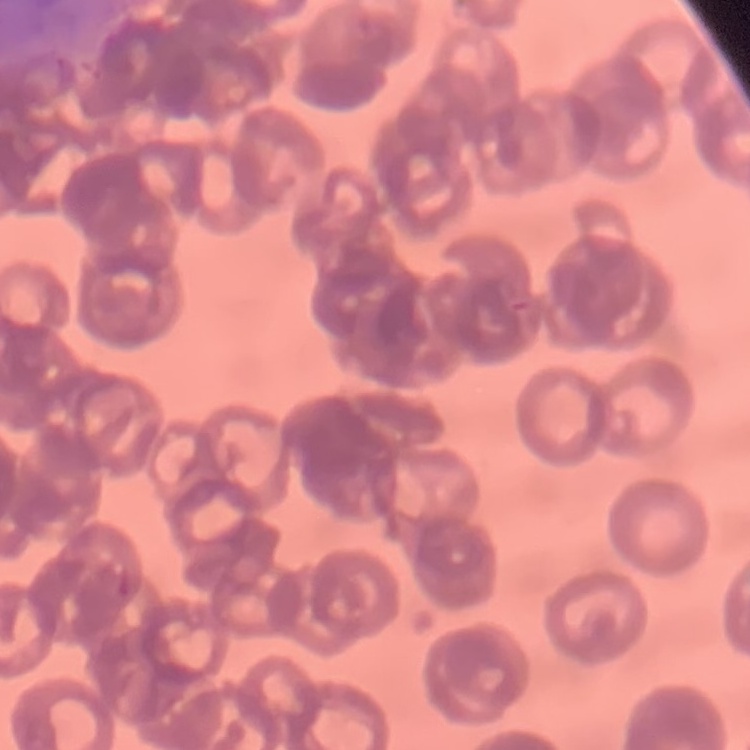
Summary:
  - Red blood cell morphology: rouleaux formation
  - Image type: one tile cut from a larger photomicrograph
  - Preparation: thin blood smear
  - Stain: Field's or Giemsa